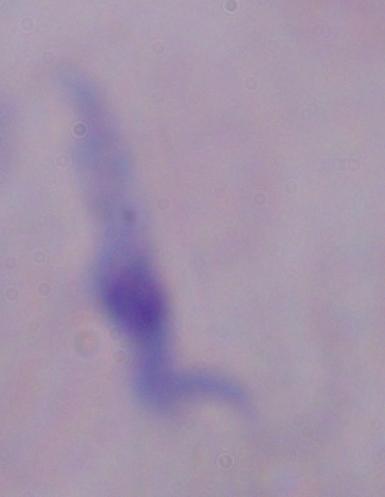
modality = photomicrograph
identification = trypanosome
magnification = 1000x